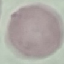 Malaria status: uninfected. Cell patch, automatically extracted from a larger field of view and resized to 64 × 64 pixels. Acquired by smartphone through the microscope eyepiece. Thin blood smear. Giemsa stain.